Classify this cell by malaria status.
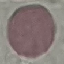
Uninfected.

Thin blood smear. Automatically extracted cell patch, resized to 64 × 64 pixels. Giemsa stain. Photographed with a smartphone camera at the microscope eyepiece.